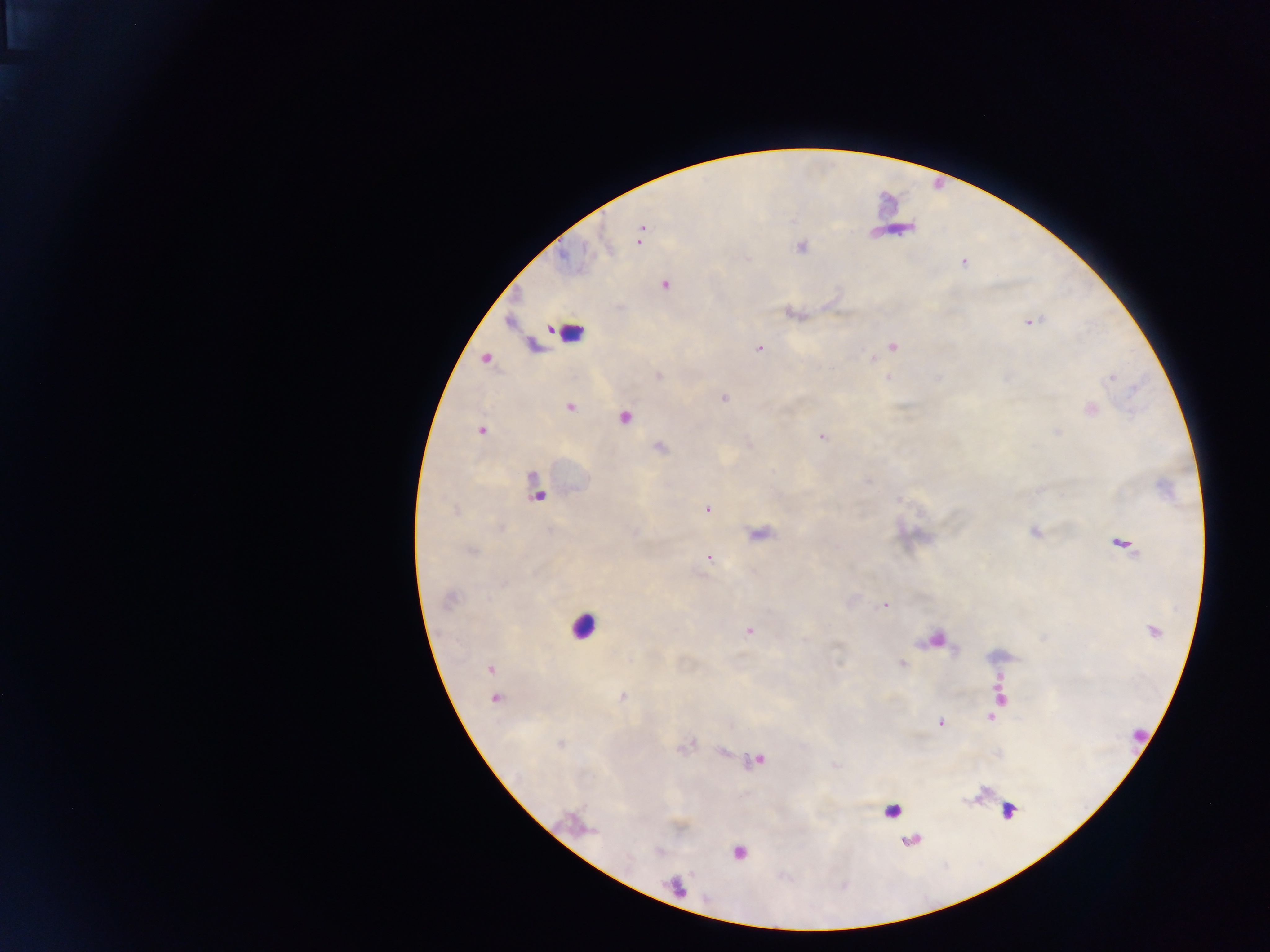

Approximate centers as [x, y] in pixels. Malaria parasite locations: [640, 236], [800, 247], [964, 263], [665, 285], [1030, 322], [892, 346], [760, 349], [658, 376], [1112, 377], [725, 399], [569, 407], [481, 431], [822, 438], [660, 448], [707, 509], [1035, 531], [1124, 544], [472, 552], [709, 557], [450, 599], [885, 605], [749, 631], [1154, 631], [902, 663], [489, 669], [622, 697], [495, 698], [1001, 699], [992, 715], [940, 722], [560, 744], [757, 761], [739, 853]. Leukocyte locations (subset; some below the resolvable size): [568, 333], [624, 422], [583, 626], [1012, 810], [893, 812]. Thick blood smear. Photographed through a microscope with a mobile-phone camera. Image is 1270×952 pixels. Collected in Ghana. One field of view.